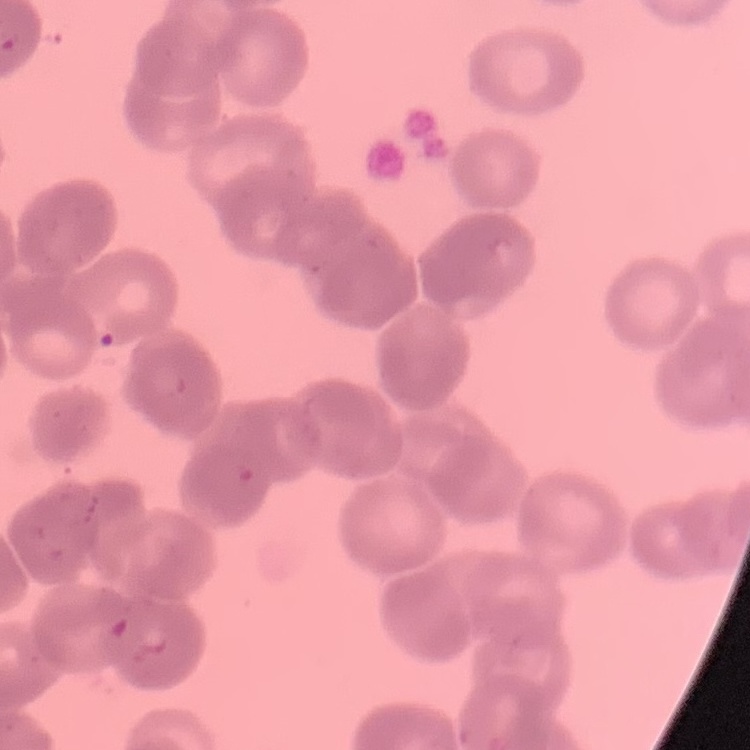

{
  "red_blood_cell_morphology": "rouleaux formation",
  "preparation": "thin blood smear",
  "image_type": "one tile cut from a larger photomicrograph",
  "stain": "Field's or Giemsa"
}